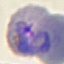

Malaria status: parasitized. Giemsa stain. Photographed with a smartphone camera at the microscope eyepiece. Thin smear of blood. Cell patch, automatically extracted from a larger field of view and resized to 64 × 64 pixels.